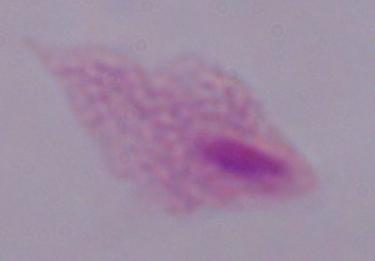
magnification = 1000x
identification = trichomonad
modality = photomicrograph